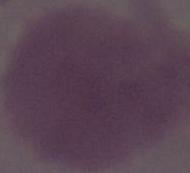
Summary:
  - Identification: red blood cell
  - Magnification: 1000x
  - Modality: micrograph